Report the malaria status of this cell.
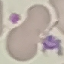

It is uninfected.

Giemsa-stained preparation. Photographed with a smartphone camera at the microscope eyepiece. Thin smear of blood. Automatically extracted cell patch, resized to 64 × 64 pixels.